Identify the blood parasite species.
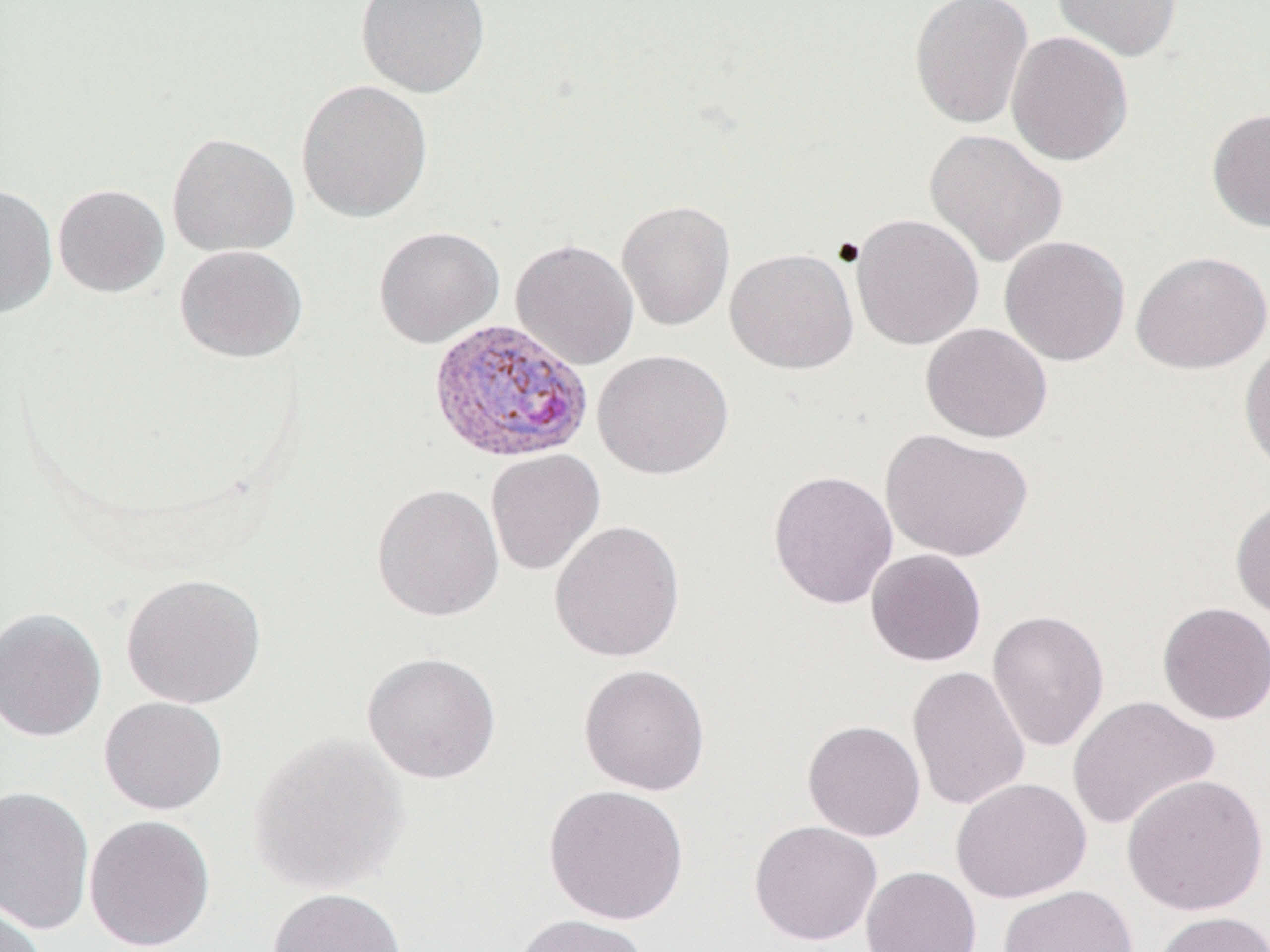
Plasmodium vivax.

Approximate bounding boxes as named x1/y1/x2/y2 corners in pixels. Plasmodium vivax-infected red blood cell locations: (x1=428, y1=317, x2=593, y2=464). Uninfected red blood cell locations: (x1=356, y1=0, x2=491, y2=98), (x1=909, y1=0, x2=1034, y2=129), (x1=1052, y1=0, x2=1181, y2=62), (x1=1006, y1=30, x2=1133, y2=166), (x1=296, y1=79, x2=433, y2=223), (x1=1206, y1=107, x2=1270, y2=233), (x1=924, y1=129, x2=1067, y2=267), (x1=166, y1=132, x2=299, y2=256), (x1=0, y1=183, x2=58, y2=319), (x1=52, y1=184, x2=170, y2=297), (x1=616, y1=199, x2=736, y2=331), (x1=850, y1=213, x2=984, y2=350), (x1=373, y1=225, x2=504, y2=348), (x1=999, y1=235, x2=1130, y2=366), (x1=511, y1=238, x2=639, y2=370), (x1=174, y1=244, x2=307, y2=363), (x1=725, y1=247, x2=859, y2=374), (x1=1131, y1=250, x2=1270, y2=374), (x1=921, y1=322, x2=1052, y2=443), (x1=1239, y1=339, x2=1270, y2=479), (x1=592, y1=349, x2=734, y2=480), (x1=879, y1=428, x2=1034, y2=563), (x1=485, y1=448, x2=606, y2=576), (x1=767, y1=469, x2=899, y2=609), (x1=372, y1=483, x2=505, y2=622), (x1=1230, y1=495, x2=1270, y2=624), (x1=548, y1=519, x2=686, y2=663), (x1=865, y1=548, x2=987, y2=667), (x1=120, y1=572, x2=266, y2=709), (x1=1157, y1=601, x2=1270, y2=725), (x1=0, y1=607, x2=107, y2=743), (x1=986, y1=609, x2=1110, y2=752), (x1=361, y1=651, x2=503, y2=784), (x1=578, y1=663, x2=711, y2=796), (x1=907, y1=665, x2=1031, y2=811), (x1=1067, y1=695, x2=1221, y2=831), (x1=98, y1=696, x2=227, y2=815), (x1=802, y1=719, x2=926, y2=842), (x1=248, y1=732, x2=410, y2=894), (x1=1121, y1=773, x2=1269, y2=916), (x1=950, y1=778, x2=1092, y2=904), (x1=543, y1=783, x2=689, y2=925), (x1=0, y1=785, x2=95, y2=935), (x1=84, y1=814, x2=216, y2=952), (x1=748, y1=819, x2=882, y2=946), (x1=861, y1=865, x2=982, y2=952), (x1=997, y1=883, x2=1139, y2=952), (x1=266, y1=886, x2=408, y2=952), (x1=0, y1=902, x2=47, y2=952), (x1=1153, y1=910, x2=1270, y2=952), (x1=511, y1=912, x2=651, y2=952). 1000x magnification. May-Grünwald-Giemsa stain. Single field of view. Optical microscopy. Image is 1270×952 pixels. Thin blood film.